Classify this cell by malaria status.
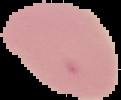
It is uninfected.

Summary:
  - Preparation: thin blood smear
  - Image type: segmented cell region on a black background
  - Image size: 121×100 pixels